Identify the parasite.
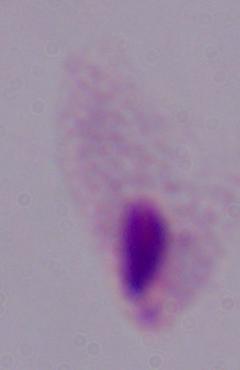

This is a trichomonad.

Photomicrograph. Captured at 1000x magnification.